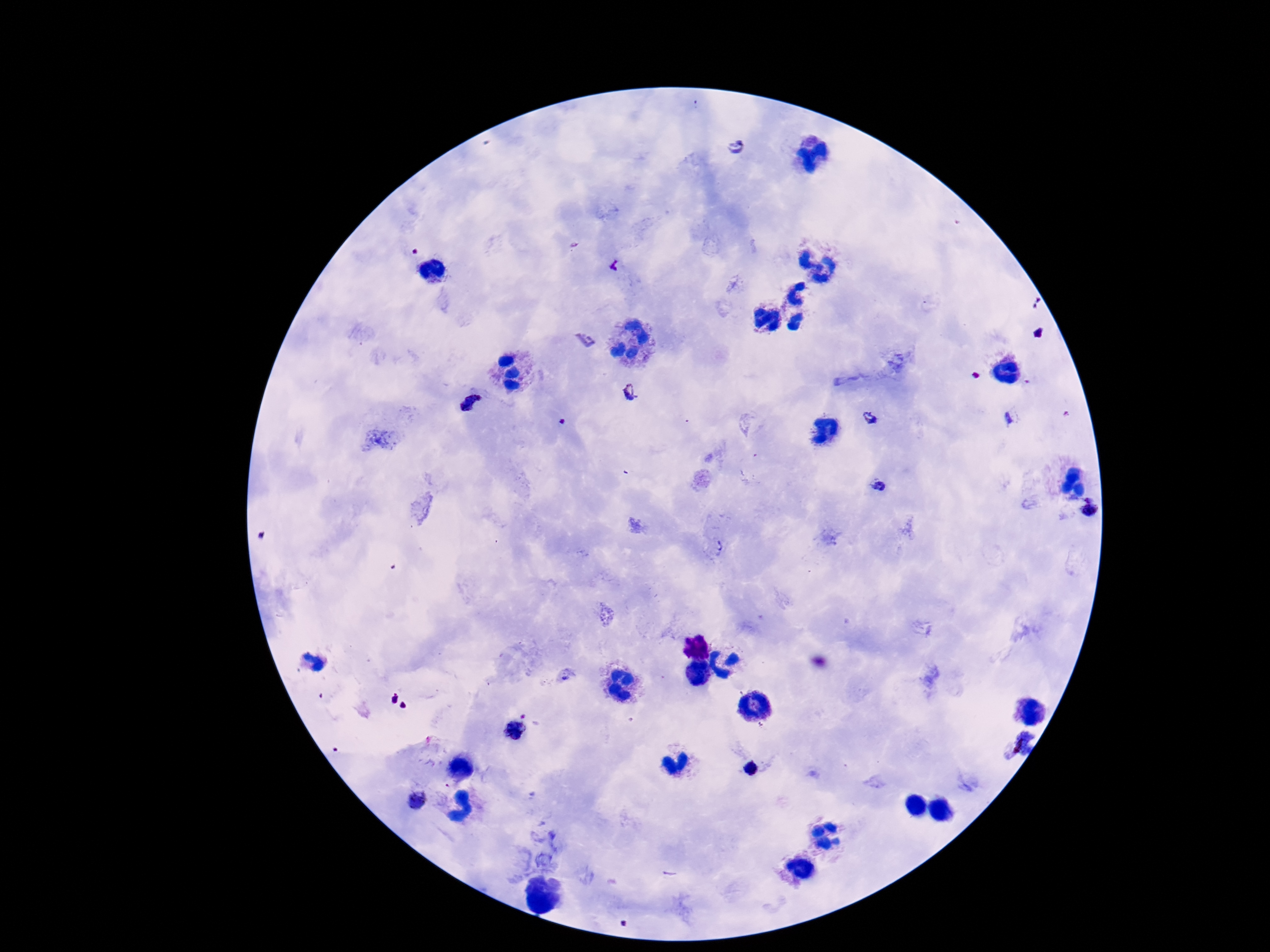

Approximate centers as [x, y] in pixels.
Summary:
  - Plasmodium parasite locations: [733, 143], [616, 266], [585, 341], [631, 395], [471, 403], [1013, 416], [872, 418], [882, 485], [1088, 507], [514, 729], [1012, 746], [751, 768], [415, 799]
  - Stain: Giemsa
  - Patient malaria status: positive
  - Magnification: 100x
  - Preparation: thick peripheral-blood smear
  - Image size: 1270×952 pixels
  - Field of view: single
  - Capture: smartphone camera through the microscope eyepiece